Identify the cell.
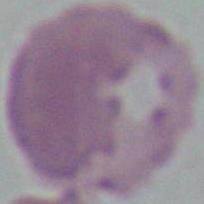

This is an erythrocyte.

magnification = 1000x
modality = photomicrograph